Identify the preparation type.
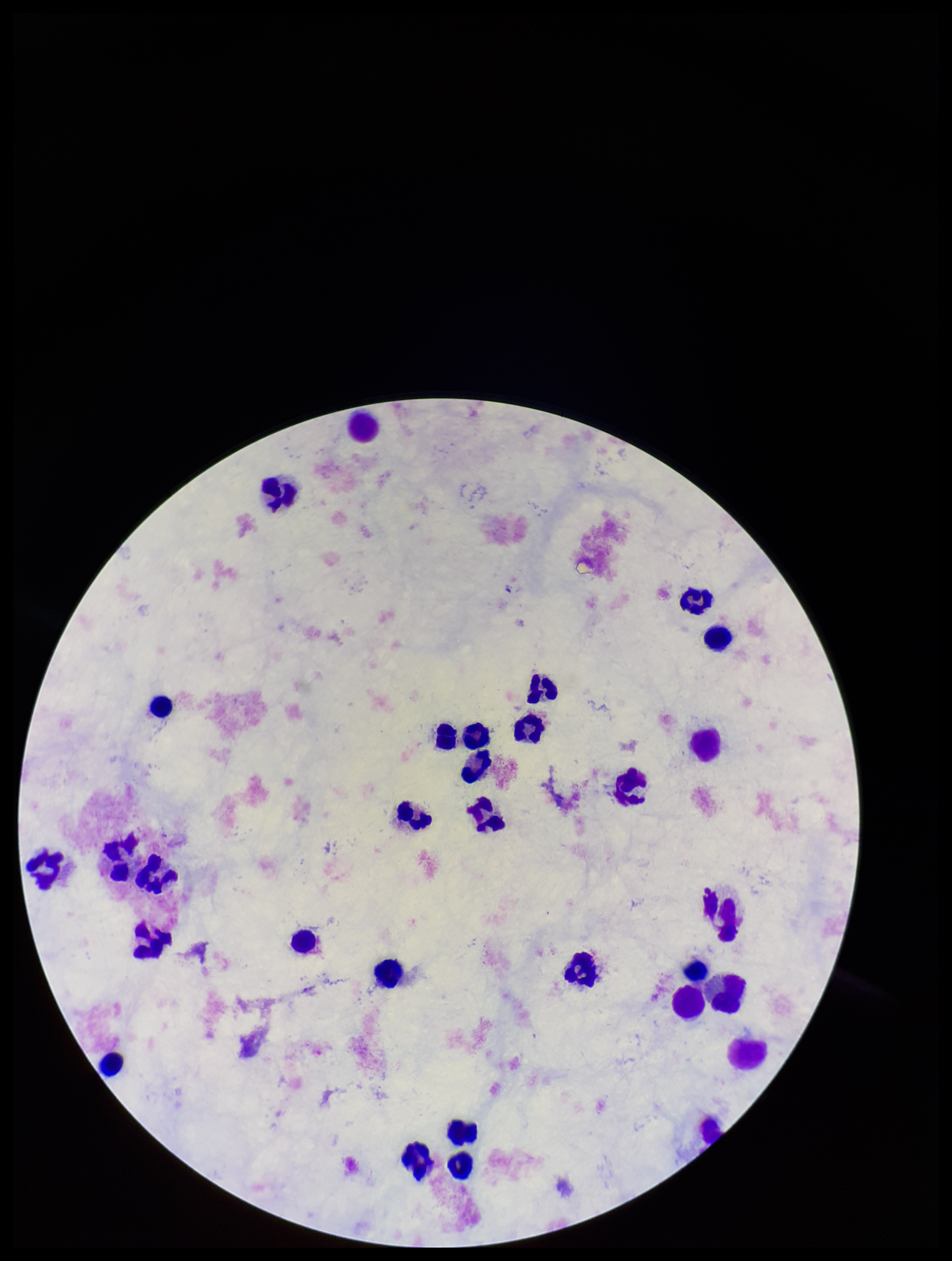
A thick smear.

stain: Giemsa
parasite_count: 0
plasmodium_parasites: none detected
image_size: 952×1261 pixels
leukocyte_count: 30
field_of_view: single
patient_malaria_status: negative
capture: smartphone photograph through the microscope eyepiece